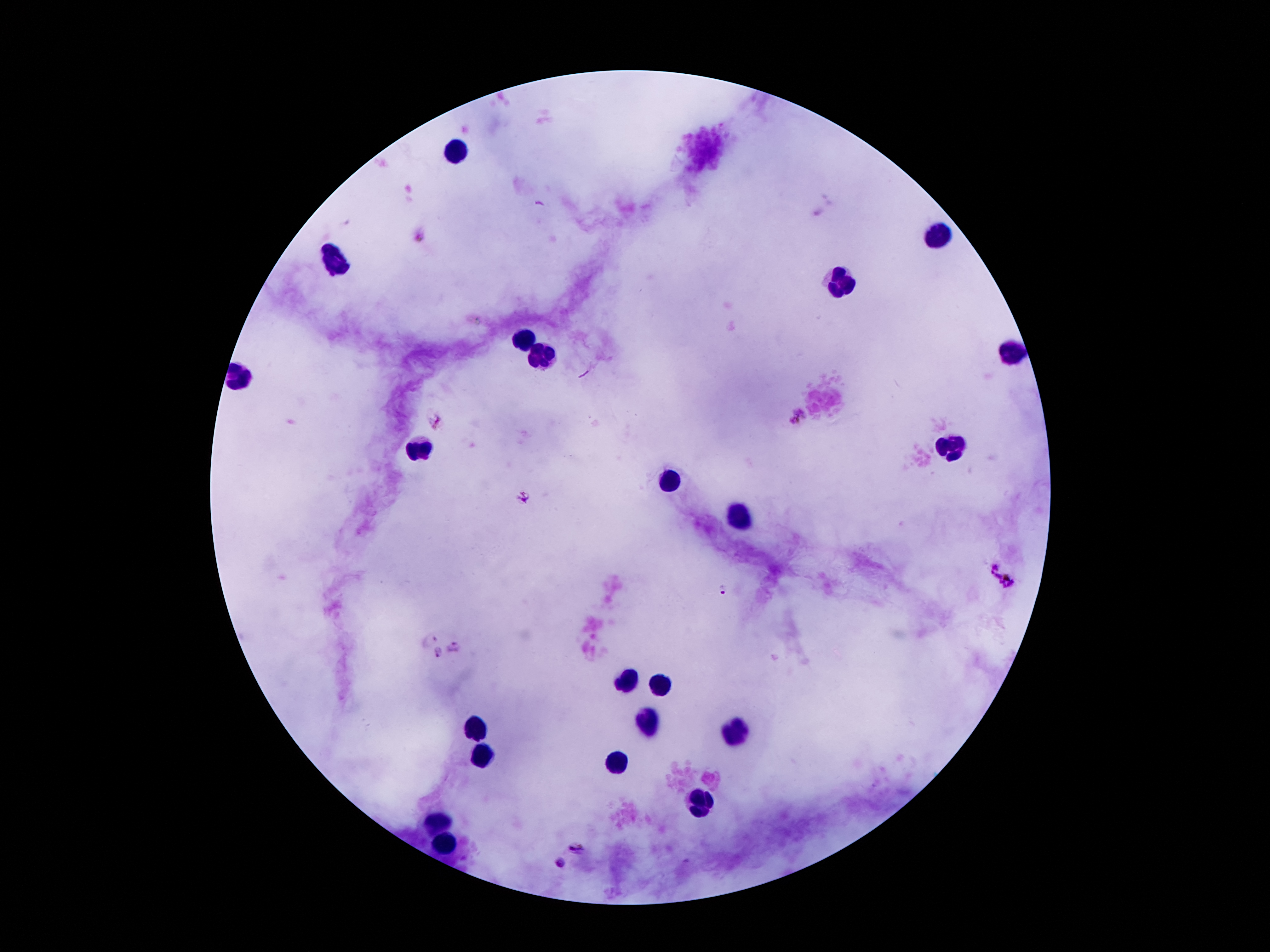

Approximate centers as {x, y} in pixels. Plasmodium parasite locations: {797, 416}, {436, 421}, {523, 497}, {990, 562}, {1004, 581}, {724, 588}, {430, 638}, {456, 644}, {438, 654}, {579, 847}, {559, 864}. Leukocyte locations: {451, 149}, {934, 235}, {341, 263}, {841, 282}, {525, 342}, {1011, 354}, {546, 356}, {241, 377}, {423, 450}, {950, 450}, {673, 480}, {738, 515}, {628, 678}, {659, 683}, {647, 720}, {476, 730}, {736, 732}, {481, 758}, {617, 765}, {701, 804}, {441, 816}, {446, 839}. One field from this slide. Thick peripheral-blood smear. Image is 1270×952 pixels. Giemsa-stained preparation. Patient malaria status: positive for Plasmodium falciparum. Smartphone photograph taken through the microscope eyepiece. 100x magnification.